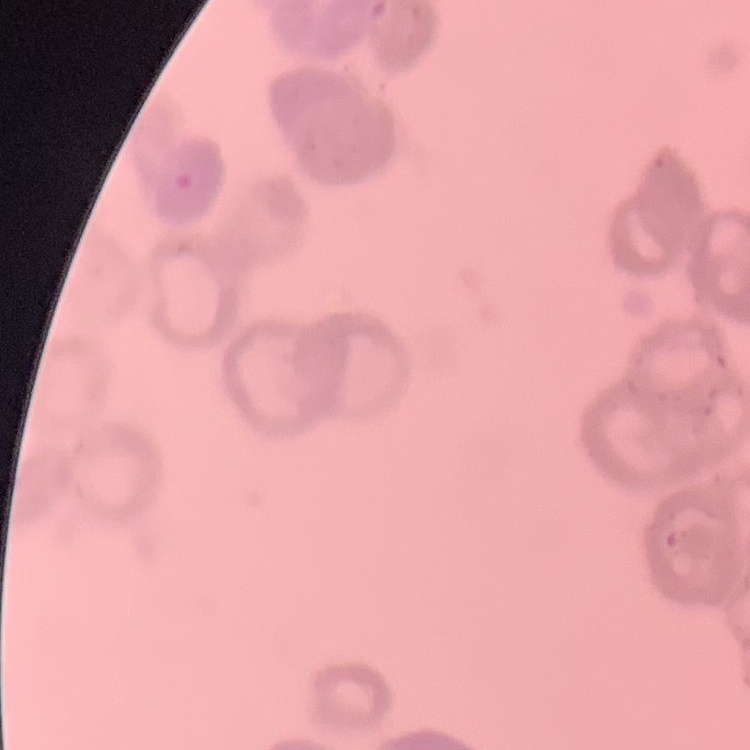

The red blood cells exhibit rouleaux formation. Field's or Giemsa stain. Square crop of a larger photomicrograph. Thin blood smear.